Name the blood parasite species.
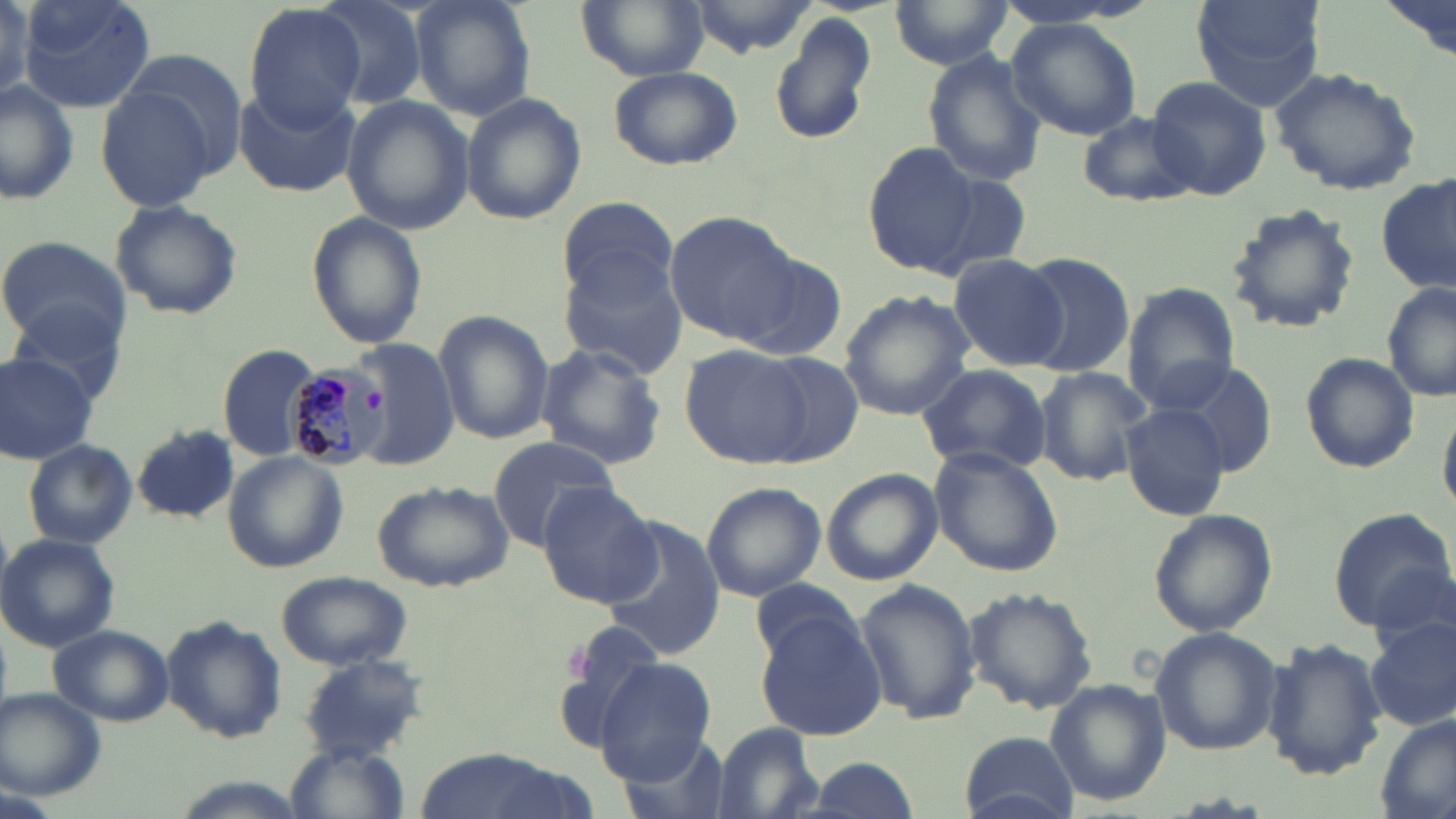

Plasmodium malariae.

Summary:
  - Coordinate format: approximate bounding boxes as (x1,y1)-(x2,y2) corner pairs in pixels
  - Uninfected red blood cell locations: (19,0)-(155,114), (311,0)-(433,110), (410,0)-(537,122), (577,0)-(709,80), (1191,0)-(1323,109), (1378,0)-(1453,61), (683,1)-(818,58), (891,2)-(1017,72), (241,3)-(368,128), (769,14)-(877,146), (1006,17)-(1143,141), (117,46)-(251,176), (919,54)-(1046,187), (608,66)-(742,171), (1270,66)-(1422,195), (1146,75)-(1272,201), (0,82)-(81,206), (95,84)-(221,212), (236,86)-(363,198), (461,94)-(585,225), (343,98)-(475,233), (1075,110)-(1202,208), (866,141)-(980,277), (930,172)-(1035,279), (1379,175)-(1455,296), (557,195)-(680,306), (109,198)-(243,321), (1224,202)-(1360,334), (666,210)-(799,343), (307,212)-(429,349), (0,234)-(130,349), (1016,251)-(1136,377), (734,252)-(847,364), (948,252)-(1068,372), (559,255)-(691,379), (1382,283)-(1456,404), (1122,285)-(1240,408), (838,291)-(973,420), (9,299)-(129,403), (434,311)-(554,445), (354,340)-(460,468), (218,344)-(323,462), (536,344)-(666,469), (681,346)-(810,467), (1299,351)-(1419,473), (0,353)-(98,463), (757,353)-(865,466), (1163,361)-(1278,477), (915,363)-(1055,476), (1034,366)-(1153,486), (1120,402)-(1229,521), (1439,410)-(1456,518), (131,424)-(240,524), (1132,428)-(1255,626), (487,436)-(618,552), (22,438)-(138,550), (928,446)-(1064,576), (221,451)-(347,572), (821,469)-(943,585), (701,481)-(826,601), (372,482)-(513,591), (536,483)-(662,608), (1327,506)-(1454,631), (1147,508)-(1277,638), (605,516)-(729,659), (2,535)-(121,652), (276,572)-(412,670), (748,577)-(864,668), (855,579)-(982,727), (965,585)-(1097,716), (756,614)-(886,741), (163,616)-(287,744), (1367,619)-(1456,733), (48,624)-(174,728), (1149,627)-(1283,758), (1261,637)-(1387,780), (299,657)-(431,760), (595,659)-(718,783), (1048,681)-(1169,806), (1,690)-(105,799), (1377,713)-(1456,819), (710,724)-(825,819), (958,732)-(1083,818), (614,734)-(734,819), (282,742)-(413,819), (417,750)-(578,819), (797,756)-(923,817)
  - Plasmodium malariae-infected red blood cell locations: (287,363)-(391,472)
  - Magnification: 1000x
  - Image size: 1456×819 pixels
  - Field of view: single
  - Modality: optical microscopy
  - Stain: May-Grünwald-Giemsa
  - Preparation: thin blood film